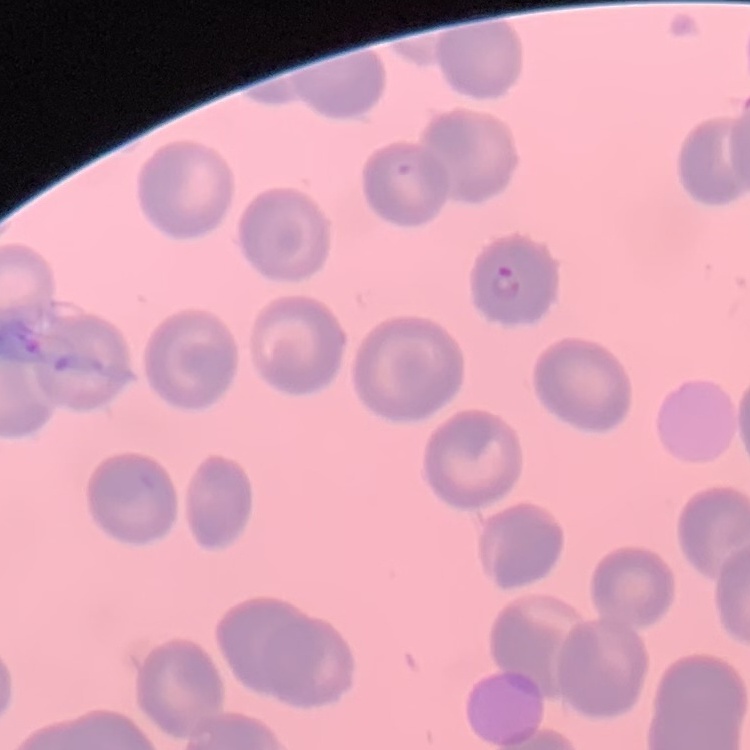
The red blood cells show no rouleaux formation. Thin blood film. Field's or Giemsa stain. Square crop of a larger photomicrograph.